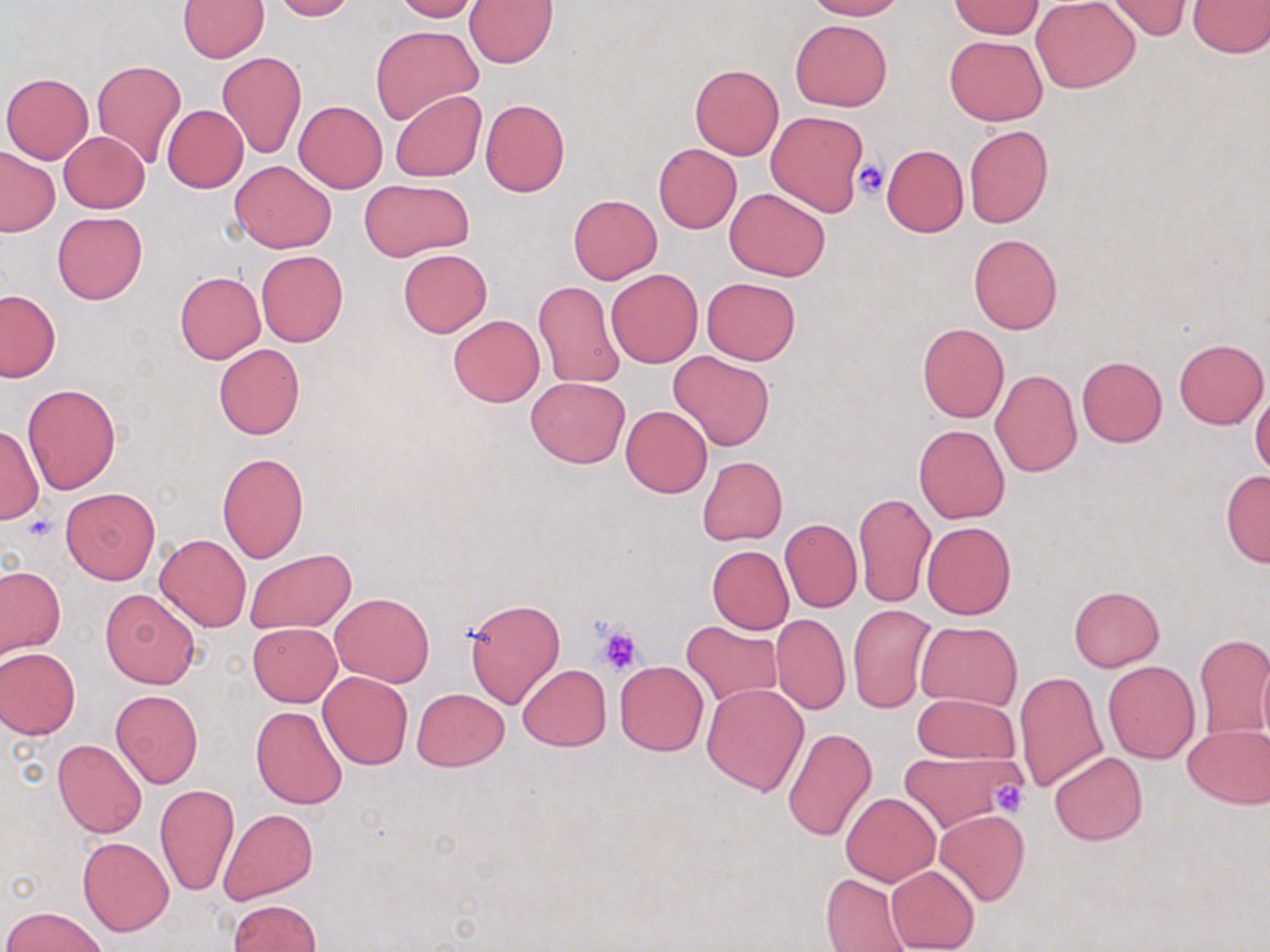 Approximate bounding boxes as (x1,y1)-(x2,y2) corner pairs in pixels. Platelet locations: (852,157)-(889,200), (591,621)-(647,676), (989,780)-(1031,819). Uninfected red blood cell locations: (178,0)-(269,61), (270,0)-(356,20), (392,0)-(481,22), (806,0)-(904,20), (1031,1)-(1141,92), (1102,1)-(1196,41), (1186,1)-(1270,56), (465,2)-(557,68), (949,2)-(1044,39), (790,18)-(891,111), (371,25)-(481,125), (944,35)-(1048,126), (217,52)-(306,157), (91,59)-(187,167), (690,63)-(783,159), (2,72)-(94,163), (389,89)-(487,181), (481,98)-(570,196), (293,100)-(388,193), (162,105)-(248,193), (766,111)-(869,216), (964,125)-(1053,229), (58,132)-(150,212), (653,143)-(742,233), (881,145)-(968,238), (0,147)-(59,236), (229,161)-(336,253), (359,180)-(473,261), (726,187)-(830,281), (568,194)-(662,284), (52,211)-(147,305), (968,233)-(1064,333), (256,249)-(348,346), (398,249)-(492,337), (606,269)-(702,367), (174,271)-(265,363), (702,277)-(800,364), (533,280)-(624,390), (0,289)-(61,382), (448,315)-(544,406), (918,322)-(1008,422), (1174,338)-(1268,429), (213,343)-(304,440), (668,351)-(775,451), (1076,356)-(1167,446), (991,369)-(1082,477), (525,376)-(630,468), (23,384)-(120,493), (1251,390)-(1270,475), (621,404)-(713,498), (1,423)-(43,526), (913,424)-(1010,523), (218,452)-(309,563), (697,456)-(787,545), (1220,470)-(1270,566), (61,488)-(160,584), (854,492)-(936,608), (780,519)-(862,612), (922,521)-(1016,619), (155,534)-(251,632), (707,545)-(793,634), (246,549)-(355,633), (124,556)-(232,668), (0,564)-(65,659), (1069,586)-(1163,672), (100,589)-(200,688), (331,591)-(433,687), (463,596)-(566,709), (847,604)-(937,713), (771,614)-(850,715), (682,622)-(782,707), (917,622)-(1021,709), (248,623)-(341,705), (1194,635)-(1270,737), (0,648)-(81,739), (1256,650)-(1270,743), (614,661)-(708,756), (1103,661)-(1199,763), (518,664)-(612,751), (317,670)-(414,769), (1014,670)-(1107,792), (702,681)-(810,796), (411,688)-(509,771), (109,690)-(203,788), (913,692)-(1019,765), (64,701)-(178,812), (251,706)-(347,809), (1181,724)-(1270,808), (783,726)-(877,841), (52,738)-(148,838), (897,750)-(1019,833), (1050,752)-(1147,845), (153,784)-(239,897), (841,792)-(940,885), (219,808)-(319,904), (934,809)-(1029,906), (77,837)-(174,936), (885,865)-(980,952), (821,873)-(914,951), (227,899)-(322,952), (3,906)-(109,952). Slide-level diagnosis: no evidence of blood parasites. Single field of view. 1000x magnification. May-Grünwald-Giemsa stain. Optical microscopy. Image is 1270×952 pixels. Thin blood film.